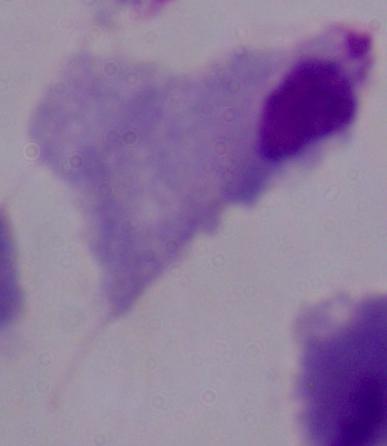

Summary:
  - Magnification: 1000x
  - Modality: photomicrograph
  - Identification: trichomonad